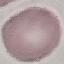
{
  "malaria_status": "uninfected",
  "capture": "smartphone camera at the microscope eyepiece",
  "stain": "Giemsa",
  "preparation": "thin blood film",
  "image_type": "automatically extracted cell patch, resized to 64 × 64 pixels"
}